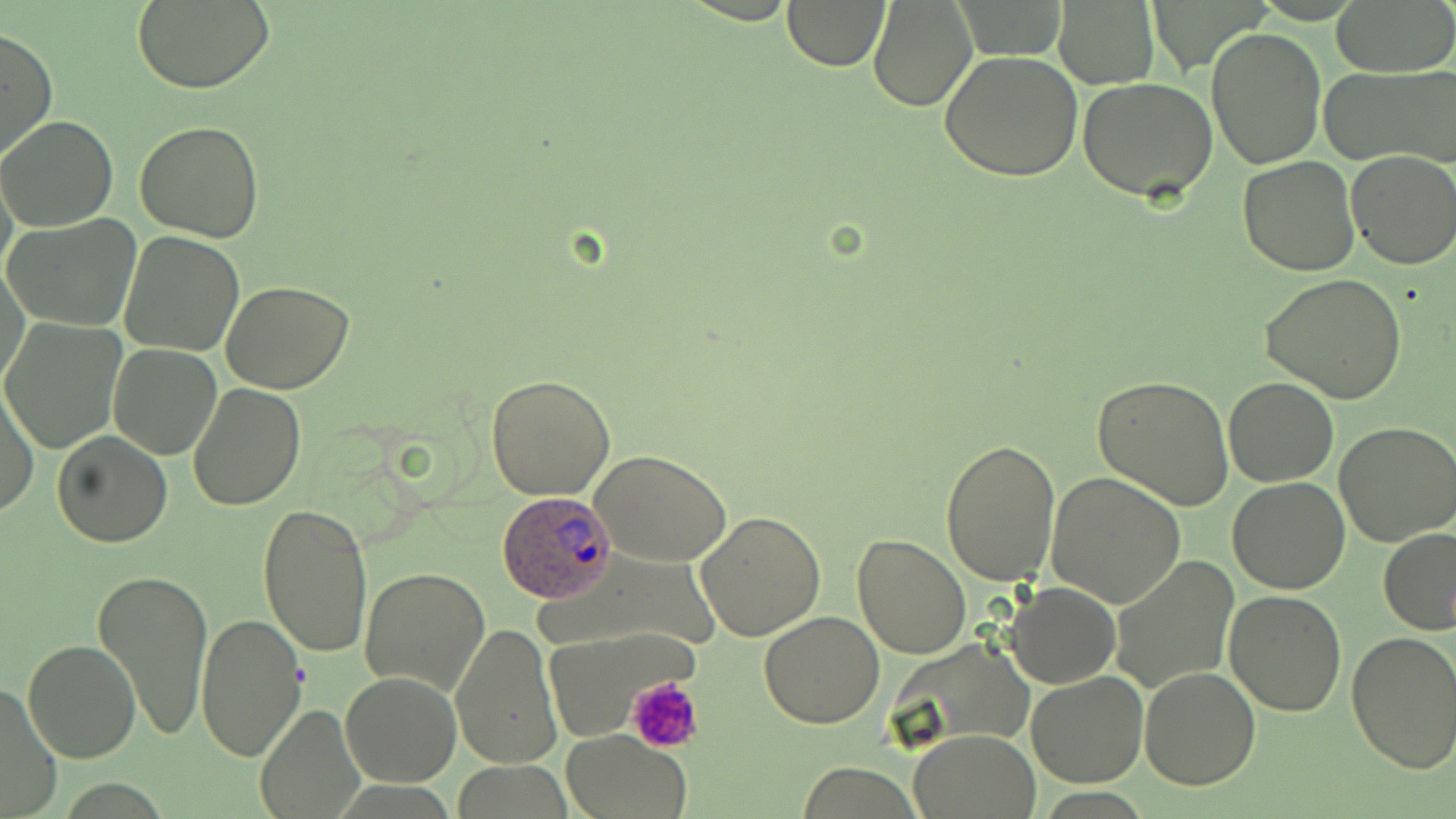

Approximate bounding boxes as (x1,y1)-(x2,y2) corner pairs in pixels. Platelet locations: (628,674)-(704,753). Plasmodium ovale-infected red blood cell locations: (494,489)-(620,601). Uninfected red blood cell locations: (782,0)-(891,71), (1331,0)-(1455,77), (868,1)-(977,113), (131,2)-(274,92), (1054,2)-(1159,88), (1206,25)-(1327,170), (0,27)-(57,162), (938,48)-(1084,181), (1321,65)-(1456,168), (1077,76)-(1218,203), (0,115)-(119,231), (135,121)-(265,241), (1345,149)-(1456,270), (1237,156)-(1360,276), (4,214)-(142,332), (117,230)-(245,357), (1,261)-(30,394), (1261,274)-(1408,403), (222,280)-(354,394), (2,319)-(126,453), (108,342)-(224,459), (485,374)-(616,500), (1092,376)-(1235,508), (1224,379)-(1337,486), (1,383)-(38,518), (187,383)-(306,513), (1334,422)-(1455,546), (52,431)-(172,547), (939,437)-(1061,585), (593,452)-(732,566), (1046,473)-(1186,610), (1228,477)-(1350,595), (258,502)-(374,660), (694,511)-(826,643), (1379,527)-(1455,634), (851,532)-(972,659), (1111,558)-(1240,694), (93,566)-(214,741), (360,567)-(490,697), (1006,582)-(1120,689), (1224,590)-(1347,714), (759,610)-(887,729), (194,613)-(309,762), (450,622)-(562,769), (1346,630)-(1456,773), (23,640)-(142,764), (1138,666)-(1261,790), (1025,670)-(1148,787), (339,672)-(462,787), (0,680)-(64,816), (255,702)-(365,817), (561,730)-(694,818), (909,730)-(1040,817). Slide-level diagnosis: Plasmodium ovale. Captured at 1000x magnification. Optical microscopy. Image is 1456×819 pixels. May-Grünwald-Giemsa stain. Thin blood smear. Single field of view.